Report the malaria status of this cell.
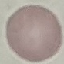

Uninfected.

Summary:
  - Image type: cell patch, automatically extracted from a larger field of view and resized to 64 × 64 pixels
  - Capture: smartphone camera at the microscope eyepiece
  - Preparation: thin blood smear
  - Stain: Giemsa